Locate every Plasmodium falciparum-infected red blood cell.
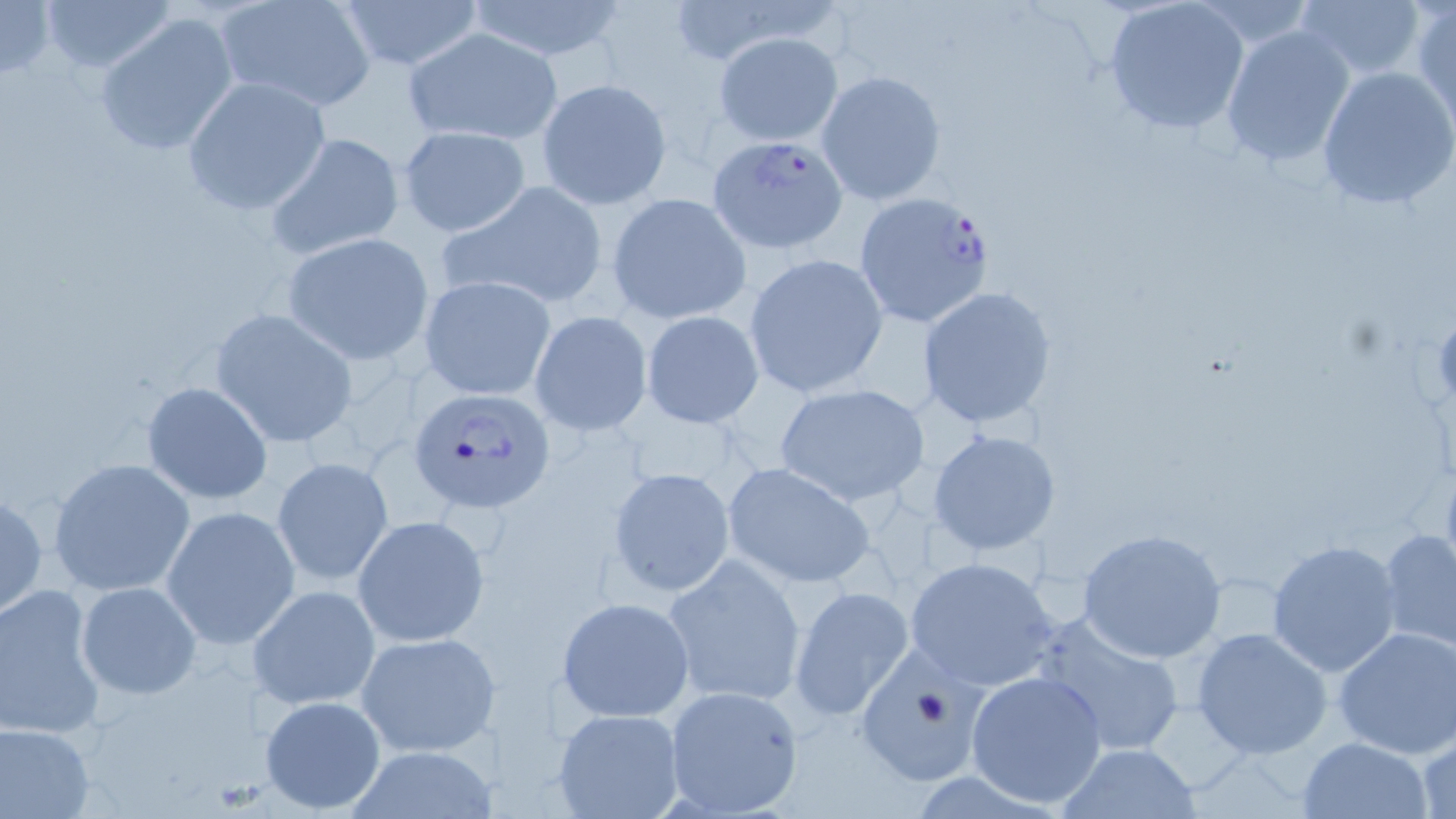

Approximate bounding boxes as (x1, y1, x2, y2) in pixels.
Plasmodium falciparum-infected red blood cells: (707, 135, 849, 254), (852, 191, 995, 329), (410, 387, 556, 514).

Uninfected red blood cell locations: (0, 0, 55, 79), (35, 0, 180, 72), (213, 0, 377, 113), (331, 0, 487, 70), (464, 1, 630, 63), (1103, 1, 1250, 136), (1296, 1, 1428, 82), (1411, 3, 1456, 129), (96, 11, 240, 156), (1219, 23, 1358, 167), (402, 28, 564, 146), (714, 31, 843, 145), (1315, 66, 1456, 210), (814, 69, 948, 207), (182, 76, 333, 217), (536, 79, 672, 208), (396, 125, 531, 237), (263, 131, 406, 261), (440, 182, 610, 311), (606, 194, 753, 326), (280, 233, 434, 363), (743, 253, 890, 400), (419, 274, 556, 400), (917, 285, 1059, 430), (209, 307, 360, 448), (640, 309, 764, 427), (529, 310, 652, 435), (139, 381, 273, 505), (772, 383, 932, 505), (927, 427, 1061, 556), (272, 456, 395, 586), (47, 457, 196, 597), (720, 460, 878, 590), (607, 466, 735, 596), (0, 489, 48, 619), (161, 506, 300, 649), (354, 515, 489, 646), (1378, 526, 1456, 653), (1077, 528, 1228, 663), (1266, 539, 1401, 676), (661, 554, 808, 707), (903, 558, 1061, 690), (0, 582, 107, 740), (75, 582, 199, 700), (248, 584, 381, 712), (789, 586, 915, 724), (556, 597, 695, 722), (1031, 612, 1187, 760), (1333, 627, 1456, 759), (1190, 628, 1333, 760), (356, 631, 498, 757), (855, 646, 1000, 787), (966, 669, 1108, 808), (661, 685, 805, 818), (260, 695, 385, 813), (552, 708, 686, 819), (0, 722, 96, 818), (1414, 733, 1456, 819), (1299, 737, 1433, 819), (1054, 742, 1202, 819), (349, 747, 492, 818). Slide-level diagnosis: Plasmodium falciparum. Captured at 1000x magnification. Image is 1456×819 pixels. May-Grünwald-Giemsa-stained preparation. Thin blood film. Light microscopy. One field of a larger specimen.